Outline each Plasmodium malariae-infected red blood cell.
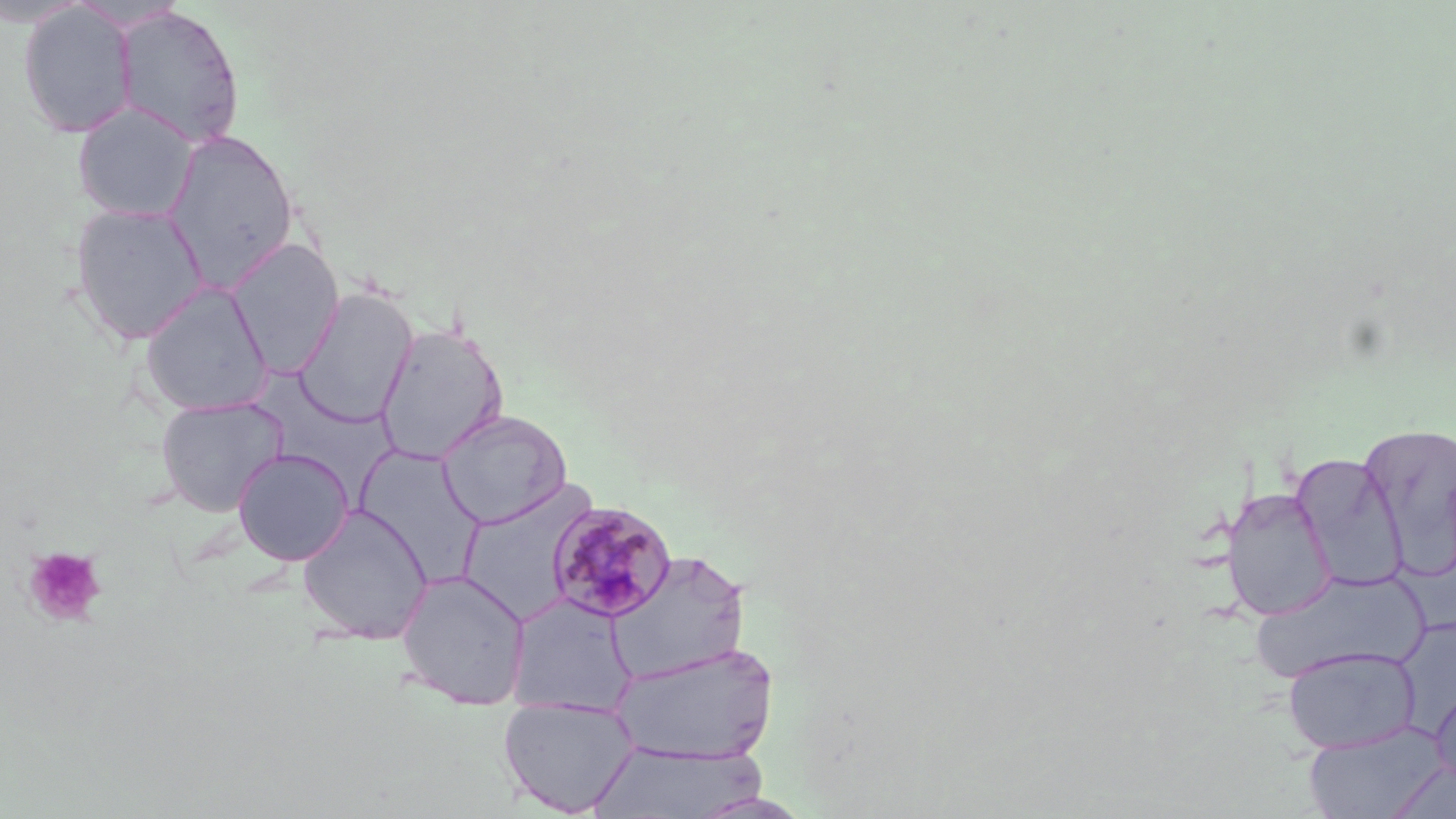

Approximate bounding boxes as (x1,y1)-(x2,y2) corner pairs in pixels.
Plasmodium malariae-infected red blood cells: (546,499)-(679,622).

Summary:
  - Platelet locations: (23,546)-(107,627)
  - Uninfected red blood cell locations: (19,2)-(137,138), (112,5)-(245,149), (72,103)-(200,222), (161,129)-(300,293), (69,202)-(209,346), (226,238)-(344,377), (138,281)-(274,417), (293,287)-(418,428), (375,322)-(509,464), (155,395)-(289,517), (437,409)-(571,528), (1358,421)-(1456,573), (233,447)-(354,565), (1291,453)-(1409,592), (456,485)-(596,624), (1220,486)-(1337,621), (296,503)-(434,645), (605,550)-(751,684), (395,568)-(532,709), (1247,568)-(1430,685), (505,594)-(634,716), (612,643)-(779,764), (1282,646)-(1420,754), (1430,686)-(1456,789), (497,695)-(639,816), (1302,723)-(1446,819), (587,740)-(765,818), (1386,761)-(1456,819)
  - Slide-level diagnosis: Plasmodium malariae
  - Stain: May-Grünwald-Giemsa
  - Field of view: single
  - Magnification: 1000x
  - Modality: light microscopy
  - Image size: 1456×819 pixels
  - Preparation: thin blood smear